Name the parasite shown.
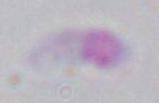

This is Toxoplasma gondii.

modality = micrograph
magnification = 1000x